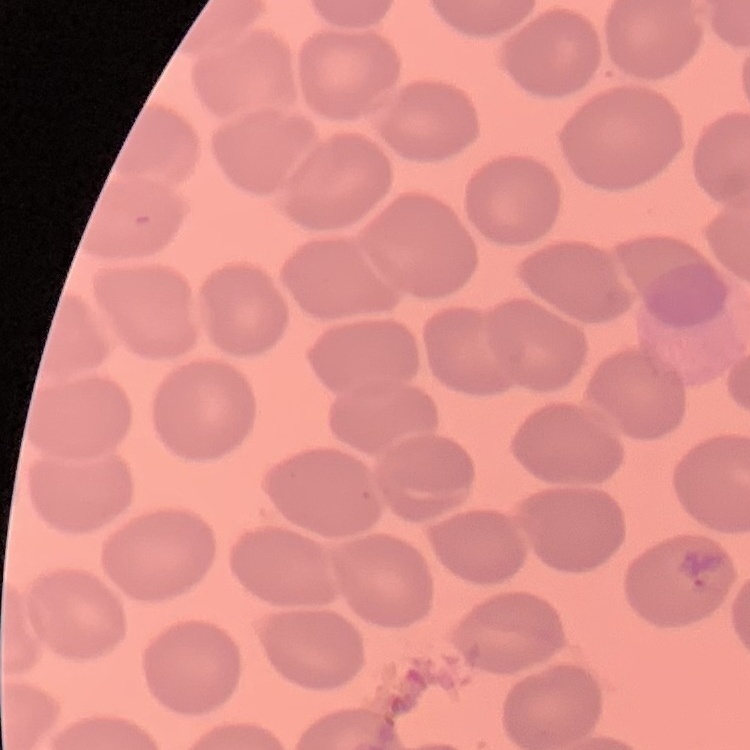

The red blood cells show no rouleaux formation. One tile cut from a larger photomicrograph. Thin blood smear. Stained with either Field's or Giemsa.